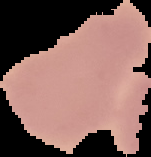
Summary:
  - Image type: cell region segmented out of the field of view; surrounding area masked to black
  - Image size: 151×157 pixels
  - Malaria status: uninfected
  - Preparation: thin blood film